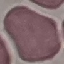 Malaria status: uninfected. Automatically extracted cell patch, resized to 64 × 64 pixels. Thin blood film. Photographed with a smartphone camera at the microscope eyepiece. Giemsa stain.